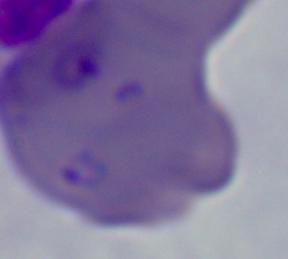

Summary:
  - Magnification: 1000x
  - Modality: micrograph
  - Identification: Babesia